Classify this cell by malaria status.
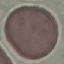
It is uninfected.

Summary:
  - Stain: Giemsa
  - Image type: automatically extracted cell patch, resized to 64 × 64 pixels
  - Capture: smartphone camera at the microscope eyepiece
  - Preparation: thin blood smear